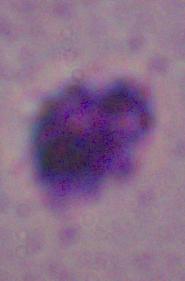

Summary:
  - Modality: photomicrograph
  - Magnification: 1000x
  - Identification: Leishmania